Report the malaria status of this cell.
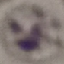
Uninfected.

capture = smartphone through the microscope eyepiece
stain = Giemsa
preparation = thin blood film
image type = cell patch, automatically extracted from a larger field of view and resized to 64 × 64 pixels